Locate every Plasmodium parasite.
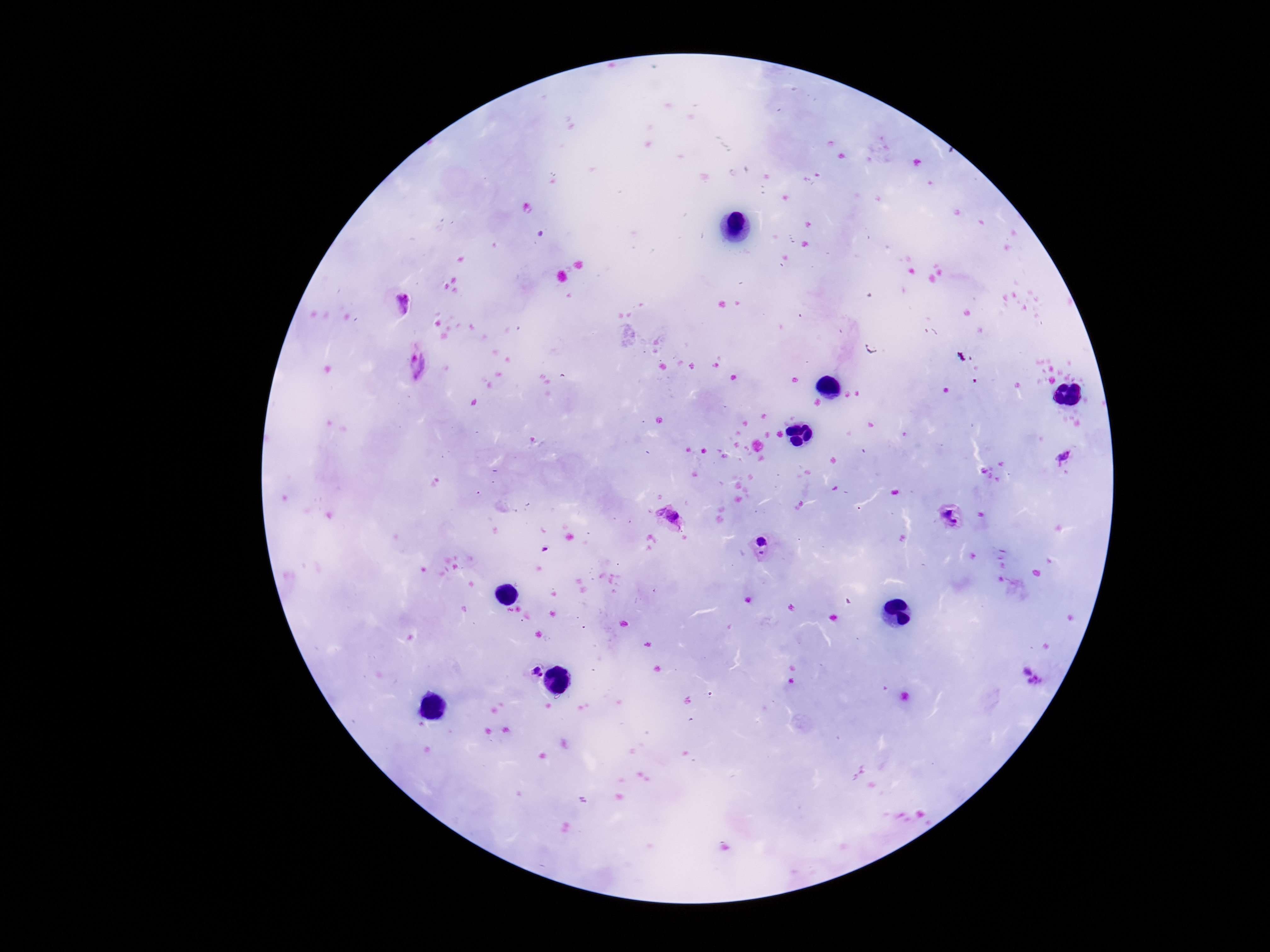
Approximate object centers, in pixels from the top-left corner.
Plasmodium parasites: (x=402, y=302), (x=416, y=367), (x=1065, y=455), (x=952, y=516), (x=672, y=518), (x=762, y=547), (x=533, y=671), (x=1031, y=676).

Summary:
  - Stain: Giemsa
  - Image size: 1270×952 pixels
  - Patient malaria status: positive
  - Preparation: thick peripheral-blood smear
  - Magnification: 100x
  - Field of view: single
  - Capture: smartphone camera through the microscope eyepiece